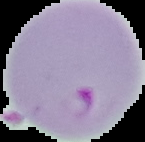

Summary:
  - Image type: segmented cell region with the area outside set to black
  - Preparation: thin blood film
  - Result: malaria parasites identified
  - Image size: 145×142 pixels